Report the malaria status of this cell.
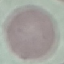

It is uninfected.

Thin blood smear. Giemsa-stained preparation. Automatically extracted cell patch, resized to 64 × 64 pixels. Acquired by smartphone through the microscope eyepiece.